Outline each blood parasite and name the species.
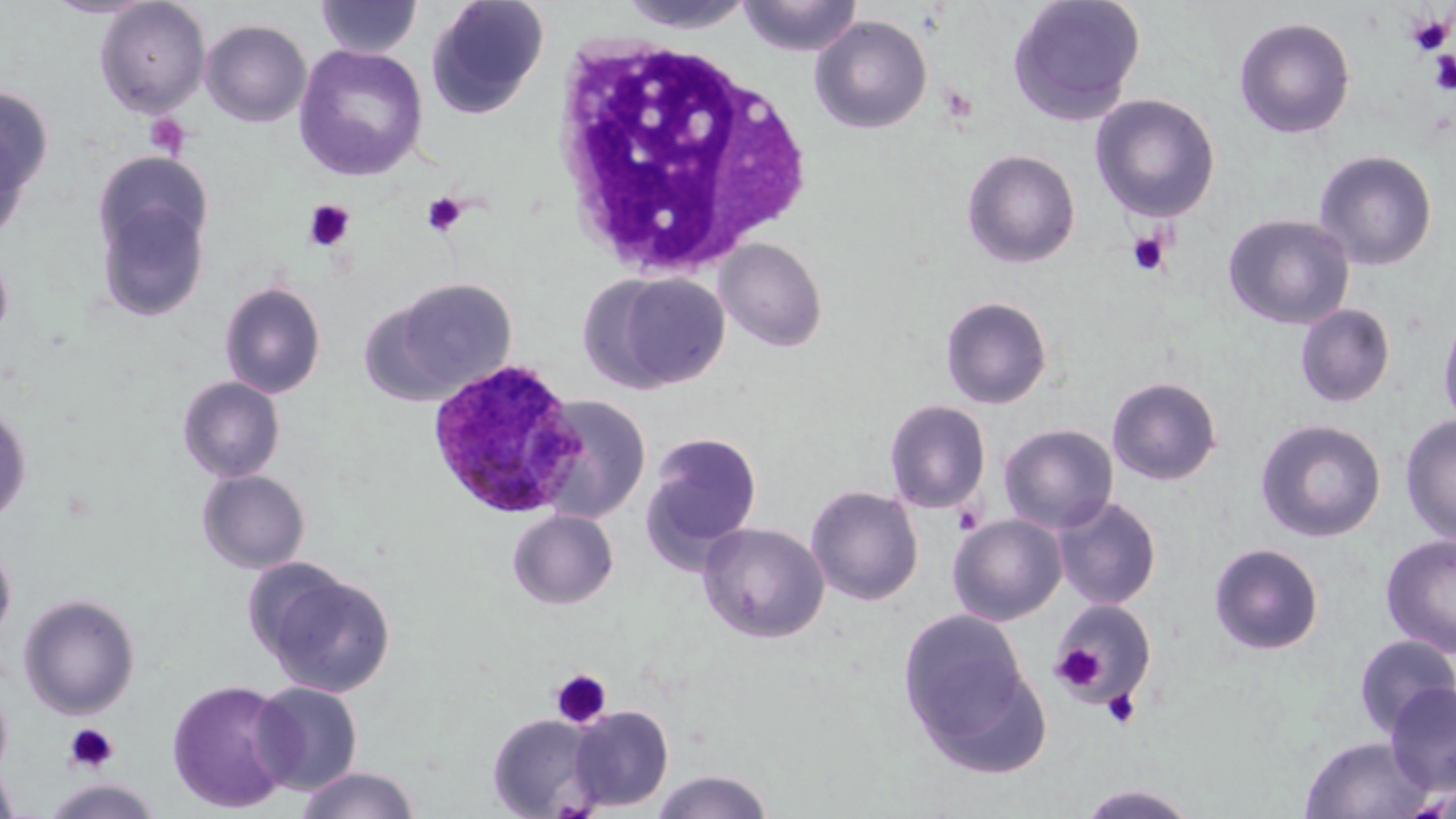

Approximate bounding boxes as [x1, y1, x2, y2] in pixels.
Plasmodium ovale-infected red blood cells: [426, 358, 585, 520].
No Plasmodium falciparum, Plasmodium malariae, Plasmodium vivax, Babesia divergens, or Trypanosoma brucei observed.

slide_level_diagnosis: Plasmodium ovale
image_size: 1456×819 pixels
platelet_locations: 'approximate bounding boxes as [x1, y1, x2, y2] in pixels: [1405, 13, 1453, 56], [1429, 50, 1456, 94], [144, 112, 191, 159], [422, 192, 467, 237], [303, 200, 355, 251], [1127, 231, 1170, 276], [953, 505, 982, 535], [1051, 642, 1107, 694], [550, 669, 613, 729], [1102, 688, 1142, 730], [63, 723, 119, 773]'
modality: optical microscopy
uninfected_red_blood_cell_locations: 'approximate bounding boxes as [x1, y1, x2, y2] in pixels: [39, 0, 159, 19], [426, 0, 550, 118], [615, 0, 760, 34], [739, 0, 863, 57], [1007, 0, 1146, 126], [94, 1, 210, 117], [315, 1, 423, 59], [809, 15, 932, 134], [1234, 16, 1356, 138], [200, 19, 312, 128], [293, 44, 429, 181], [0, 83, 53, 212], [1090, 93, 1221, 222], [0, 121, 31, 246], [961, 149, 1081, 268], [1314, 150, 1438, 270], [92, 152, 213, 263], [95, 196, 210, 322], [1223, 213, 1355, 330], [714, 237, 828, 352], [0, 245, 14, 350], [589, 271, 731, 393], [372, 276, 519, 403], [219, 282, 326, 399], [940, 295, 1052, 409], [1295, 304, 1396, 407], [1437, 306, 1456, 433], [177, 376, 286, 482], [1107, 376, 1223, 486], [533, 395, 651, 521], [884, 399, 991, 513], [0, 401, 32, 526], [1400, 414, 1456, 546], [1255, 419, 1386, 542], [998, 423, 1119, 533], [644, 432, 763, 558], [197, 470, 310, 573], [806, 485, 923, 606], [1052, 495, 1162, 610], [507, 509, 619, 609], [948, 513, 1067, 625], [697, 521, 831, 643], [1380, 534, 1456, 659], [0, 537, 16, 651], [1208, 542, 1325, 655], [258, 565, 395, 698], [19, 595, 140, 719], [1053, 600, 1158, 701], [897, 609, 1030, 745], [1354, 634, 1455, 738], [910, 653, 1054, 782], [167, 679, 297, 813], [251, 681, 363, 796], [1385, 683, 1456, 797], [568, 705, 673, 812], [487, 713, 604, 818], [1299, 736, 1431, 819], [0, 765, 19, 818], [295, 766, 420, 819], [651, 770, 775, 819], [43, 779, 163, 818], [1078, 784, 1200, 819]'
preparation: thin blood film
magnification: 1000x
field_of_view: one of a larger specimen
stain: May-Grünwald-Giemsa
white_blood_cell_locations: 'approximate bounding boxes as [x1, y1, x2, y2] in pixels: [550, 33, 813, 280]'